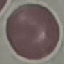
Summary:
  - Malaria status: uninfected
  - Capture: smartphone through the microscope eyepiece
  - Image type: cell patch, automatically extracted from a larger field of view and resized to 64 × 64 pixels
  - Preparation: thin smear
  - Stain: Giemsa